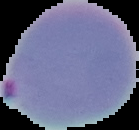

image type = cell region segmented out of the field of view; surrounding area masked to black
result = malaria parasites detected
image size = 139×130 pixels
preparation = thin blood film